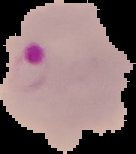

Summary:
  - Preparation: thin blood smear
  - Image type: segmented cell region on a black background
  - Malaria status: parasitized
  - Image size: 136×154 pixels